Give the position of every Plasmodium parasite.
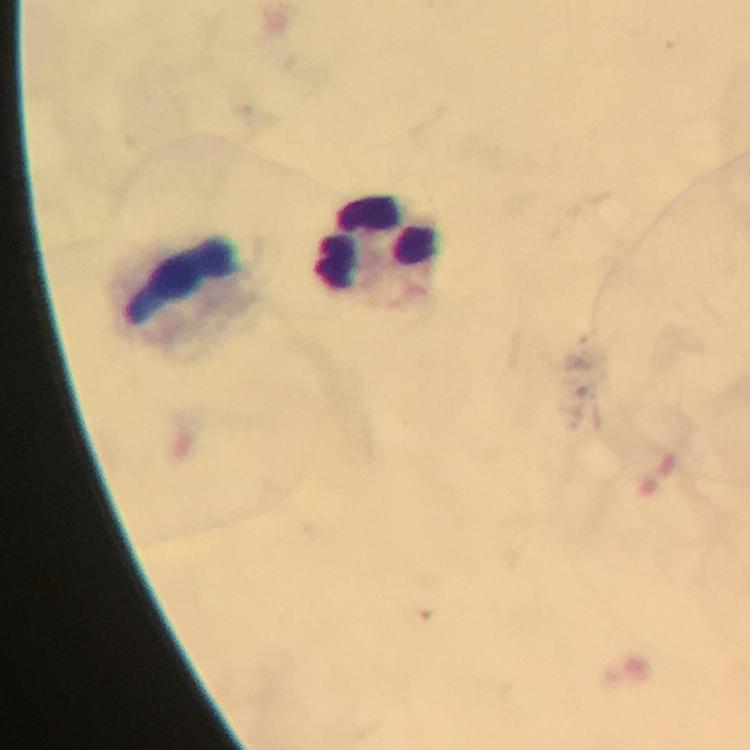
No Plasmodium parasites seen.

Approximate centers as [x, y] in pixels.
Summary:
  - Leukocyte locations: [381, 246], [186, 280]
  - Cropped from: one field of view
  - Capture: smartphone mounted on the microscope
  - Immersion oil: used
  - Context: from a diagnostic examination for malaria
  - Image size: 750×750 pixels
  - Stain: Giemsa
  - Magnification: 100x
  - Preparation: thick blood film